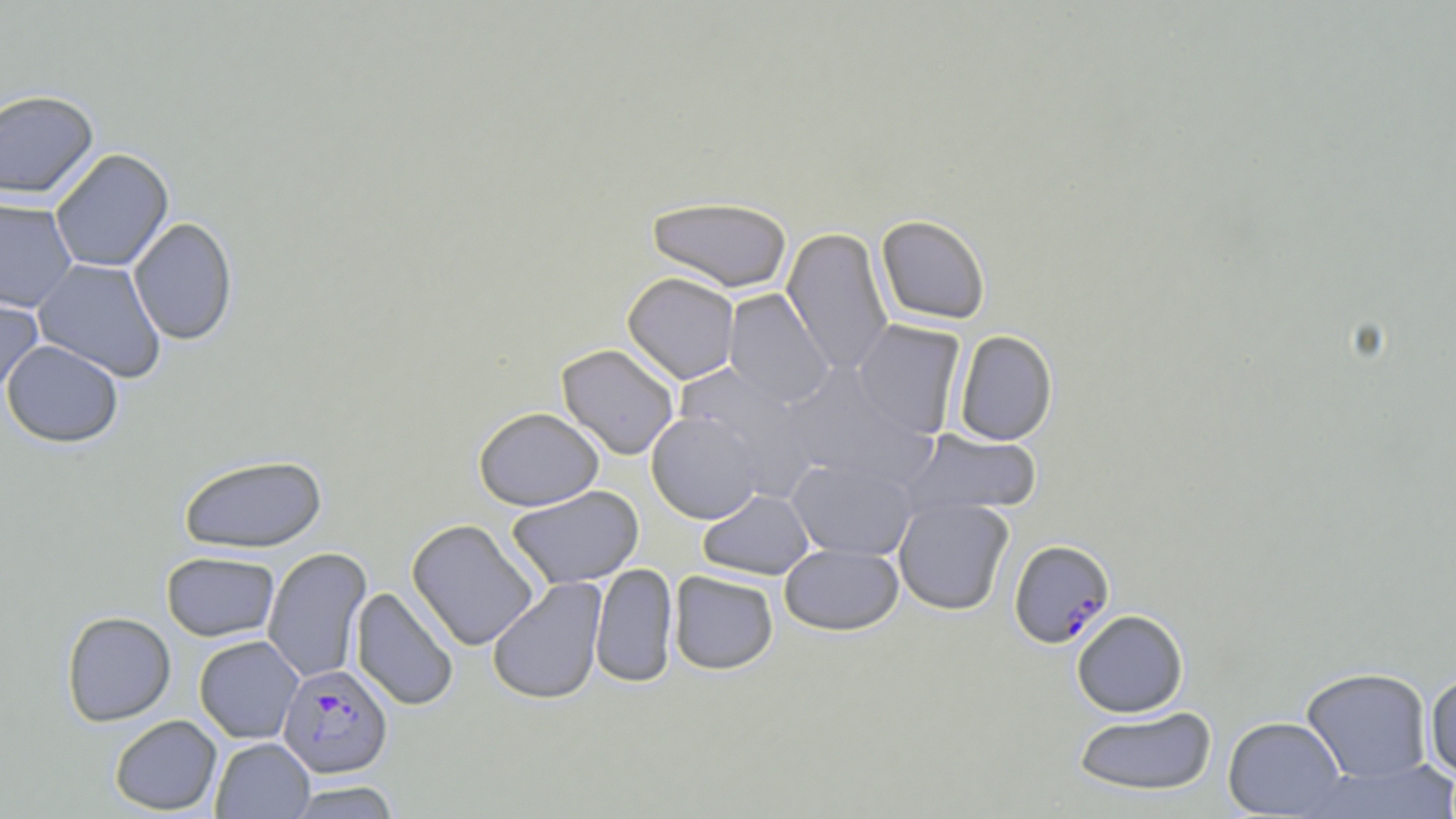 Approximate bounding boxes as named x1/y1/x2/y2 corners in pixels. Uninfected red blood cell locations: (x1=0, y1=89, x2=99, y2=200), (x1=49, y1=148, x2=174, y2=273), (x1=647, y1=196, x2=793, y2=293), (x1=0, y1=198, x2=78, y2=312), (x1=875, y1=215, x2=991, y2=325), (x1=128, y1=216, x2=238, y2=346), (x1=782, y1=228, x2=895, y2=376), (x1=32, y1=258, x2=167, y2=383), (x1=622, y1=272, x2=740, y2=385), (x1=0, y1=287, x2=44, y2=399), (x1=723, y1=288, x2=834, y2=408), (x1=852, y1=319, x2=966, y2=439), (x1=953, y1=330, x2=1058, y2=446), (x1=1, y1=339, x2=124, y2=447), (x1=556, y1=343, x2=680, y2=460), (x1=674, y1=363, x2=815, y2=496), (x1=779, y1=363, x2=934, y2=490), (x1=473, y1=406, x2=604, y2=511), (x1=646, y1=411, x2=762, y2=524), (x1=900, y1=429, x2=1042, y2=520), (x1=178, y1=454, x2=328, y2=553), (x1=787, y1=457, x2=919, y2=561), (x1=506, y1=485, x2=644, y2=589), (x1=698, y1=489, x2=815, y2=580), (x1=893, y1=498, x2=1014, y2=615), (x1=406, y1=519, x2=540, y2=651), (x1=779, y1=543, x2=904, y2=635), (x1=262, y1=547, x2=372, y2=684), (x1=161, y1=551, x2=280, y2=641), (x1=590, y1=563, x2=678, y2=689), (x1=668, y1=571, x2=779, y2=675), (x1=487, y1=577, x2=608, y2=706), (x1=351, y1=587, x2=459, y2=712), (x1=1071, y1=609, x2=1189, y2=717), (x1=61, y1=611, x2=176, y2=726), (x1=194, y1=635, x2=304, y2=743), (x1=1301, y1=666, x2=1433, y2=783), (x1=1424, y1=672, x2=1456, y2=780), (x1=1073, y1=706, x2=1217, y2=797), (x1=109, y1=715, x2=222, y2=815), (x1=1223, y1=716, x2=1346, y2=817), (x1=210, y1=737, x2=314, y2=818), (x1=1304, y1=759, x2=1455, y2=818), (x1=285, y1=780, x2=403, y2=818). Plasmodium falciparum-infected red blood cell locations: (x1=1008, y1=539, x2=1115, y2=649), (x1=277, y1=663, x2=393, y2=778). Slide-level diagnosis: Plasmodium falciparum. One field of a larger specimen. Image is 1456×819 pixels. Light microscopy. 1000x magnification. Thin blood smear. May-Grünwald-Giemsa-stained preparation.